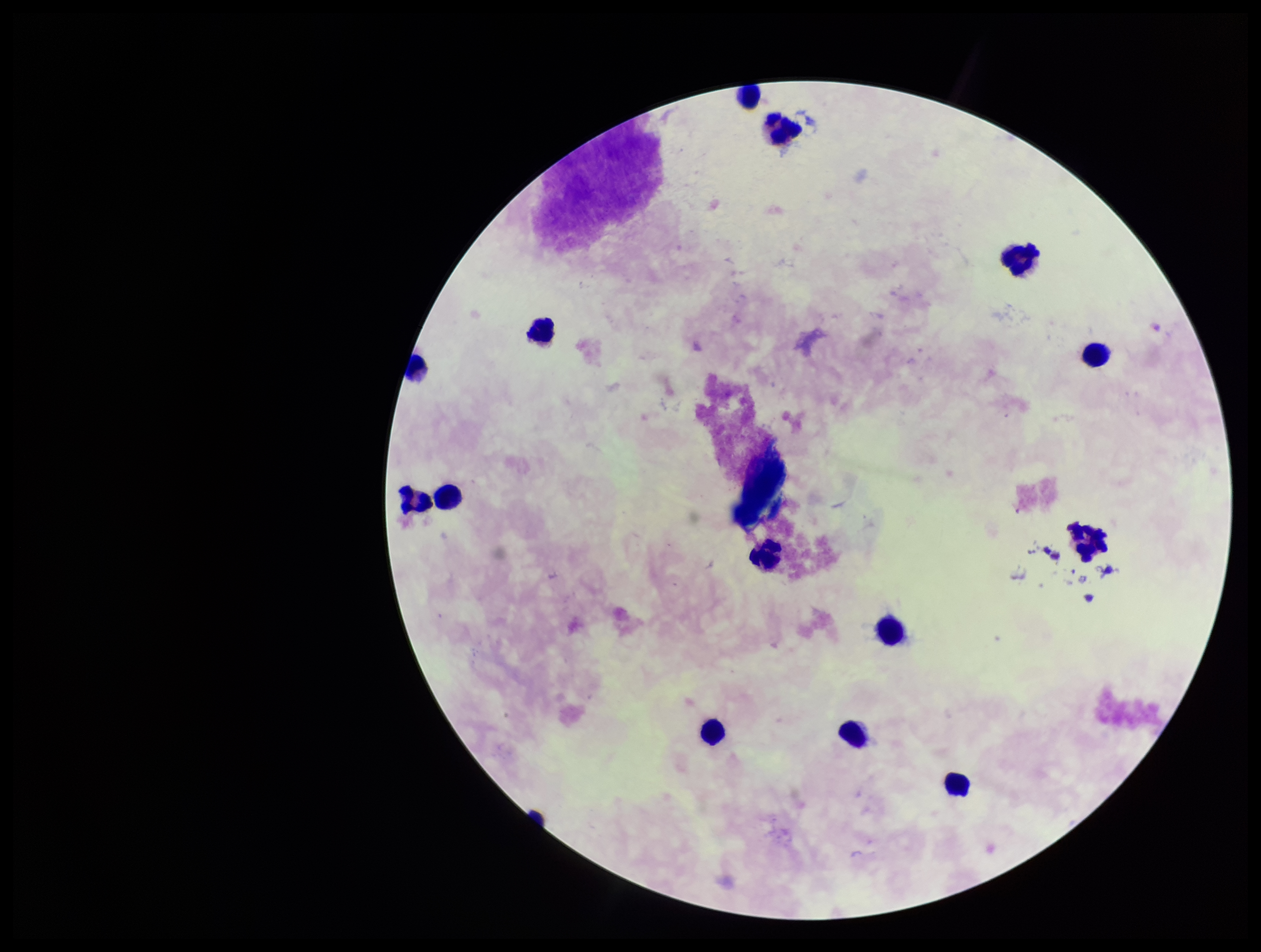

One field from this slide. Patient malaria status: negative. Preparation: thick blood smear. Image is 1261×952 pixels. Photographed through the microscope eyepiece with a smartphone camera. Plasmodium parasites: none detected. Stained with Giemsa. Parasite count: 0. Leukocyte count: 13.